Assess the morphology of the erythrocytes.
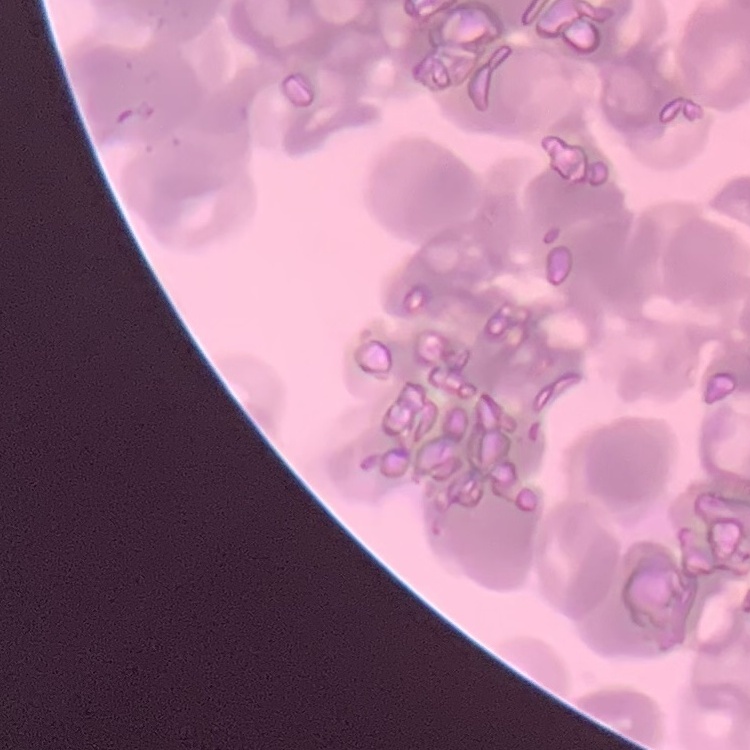

They show rouleaux formation.

preparation = thin peripheral smear
image type = square crop of a larger photomicrograph
stain = Field's or Giemsa